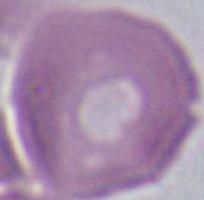

{
  "magnification": "1000x",
  "modality": "photomicrograph",
  "identification": "red blood cell"
}